Outline each Plasmodium malariae-infected red blood cell.
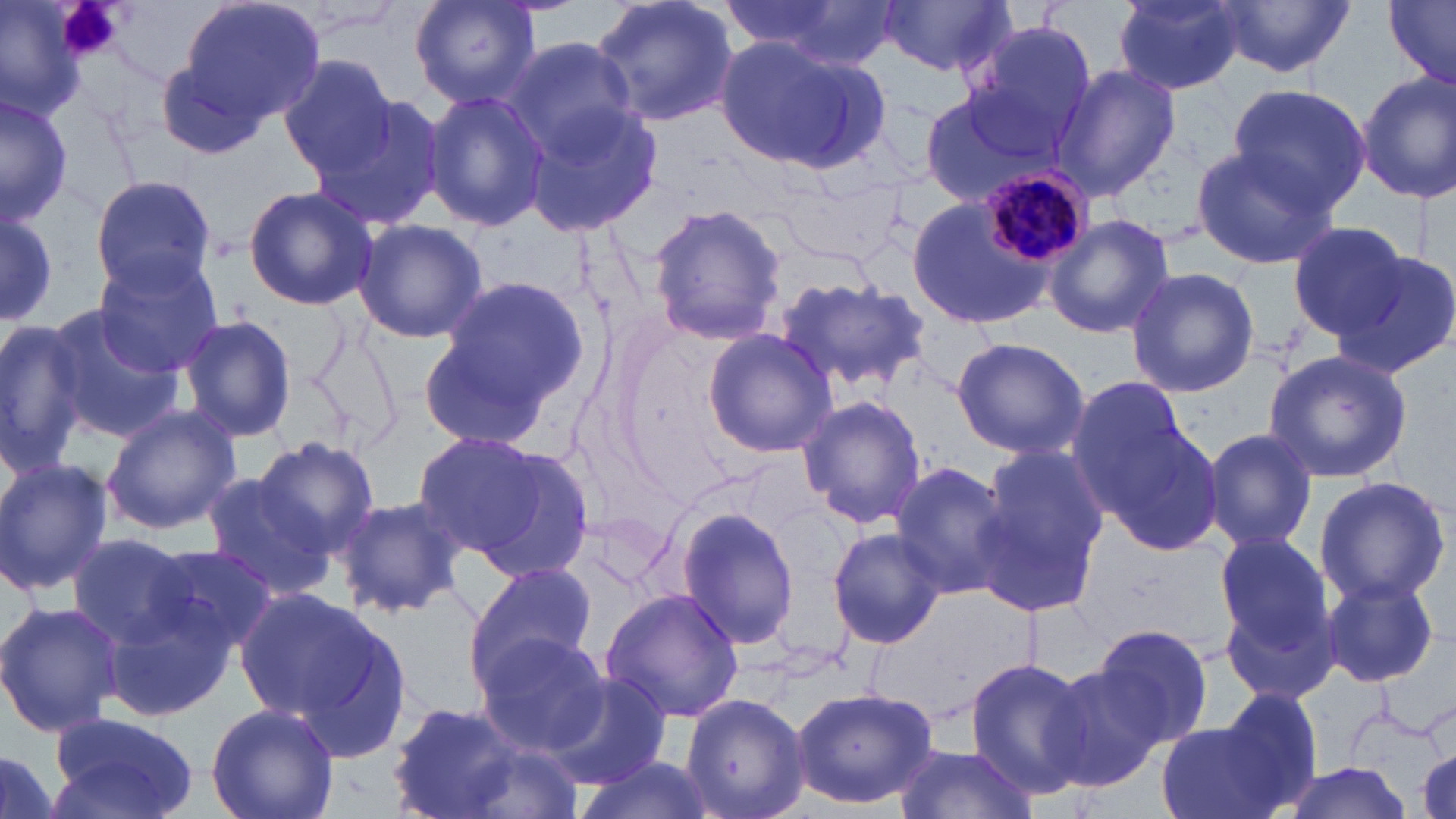
Approximate bounding boxes as (x1, y1, x2, y2) in pixels.
Plasmodium malariae-infected red blood cells: (978, 168, 1091, 266).

slide-level diagnosis = Plasmodium malariae
platelet locations = approximate bounding boxes as (x1, y1, x2, y2) in pixels: (55, 0, 121, 60)
stain = May-Grünwald-Giemsa
modality = optical microscopy
preparation = thin blood smear
magnification = 1000x
uninfected red blood cell locations = approximate bounding boxes as (x1, y1, x2, y2) in pixels: (0, 0, 85, 119), (177, 0, 327, 124), (409, 0, 541, 110), (586, 0, 741, 130), (728, 0, 903, 68), (1114, 0, 1250, 93), (1212, 0, 1355, 76), (1383, 0, 1456, 87), (878, 2, 1018, 76), (967, 19, 1097, 148), (714, 36, 889, 173), (503, 37, 641, 160), (153, 54, 279, 163), (278, 55, 401, 180), (1053, 62, 1180, 201), (1354, 70, 1456, 206), (1227, 81, 1371, 211), (918, 85, 1070, 208), (422, 89, 550, 232), (0, 90, 73, 228), (305, 92, 448, 234), (519, 96, 664, 237), (1188, 144, 1341, 272), (88, 175, 218, 300), (243, 185, 378, 311), (906, 190, 1062, 334), (647, 204, 787, 345), (0, 211, 59, 324), (1042, 214, 1175, 340), (352, 218, 487, 345), (1289, 221, 1412, 341), (1333, 250, 1456, 379), (92, 251, 224, 375), (1124, 266, 1260, 397), (433, 273, 590, 421), (773, 275, 931, 398), (40, 302, 186, 442), (303, 313, 407, 448), (180, 314, 296, 444), (0, 317, 92, 476), (416, 321, 566, 455), (704, 328, 838, 458), (951, 337, 1089, 460), (1261, 349, 1411, 485), (1069, 383, 1216, 553), (797, 394, 925, 530), (100, 403, 240, 535), (1202, 426, 1318, 555), (410, 430, 570, 567), (253, 437, 383, 558), (971, 448, 1105, 617), (0, 456, 113, 598), (889, 459, 1016, 598), (198, 475, 338, 600), (1311, 475, 1451, 608), (331, 493, 470, 621), (677, 506, 803, 651), (826, 527, 947, 649), (1213, 530, 1337, 661), (66, 533, 198, 647), (141, 544, 281, 657), (468, 560, 598, 683), (1319, 575, 1442, 688), (236, 586, 403, 743), (94, 587, 239, 721), (600, 587, 745, 723), (0, 600, 123, 739), (1092, 623, 1213, 749), (474, 631, 610, 755), (965, 657, 1096, 800), (1041, 664, 1166, 792), (546, 671, 670, 790), (790, 685, 939, 809), (1214, 687, 1323, 807), (680, 693, 809, 819), (385, 701, 531, 817), (206, 702, 339, 819), (48, 711, 200, 819), (1155, 715, 1298, 819), (1414, 731, 1455, 819), (893, 744, 1039, 819), (0, 745, 66, 819), (573, 752, 712, 819), (1274, 763, 1415, 819)
image size = 1456×819 pixels
field of view = one of a larger specimen